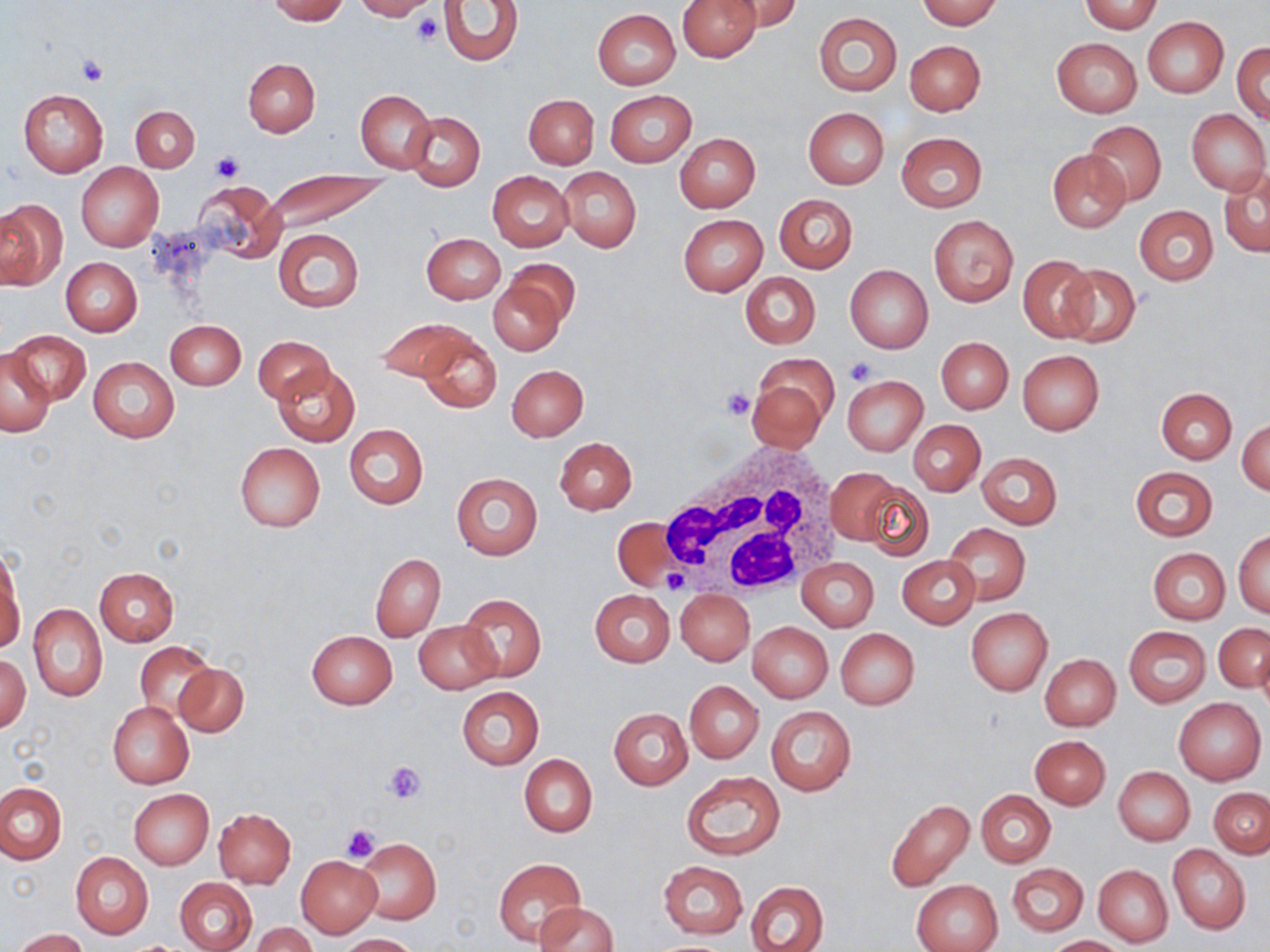 Approximate bounding boxes as [x1, y1, x2, y2] in pixels. White blood cell locations: [656, 441, 848, 603]. Platelet locations: [410, 12, 443, 45], [75, 55, 109, 87], [209, 152, 243, 184], [846, 356, 878, 383], [721, 389, 755, 422], [662, 571, 689, 594], [385, 762, 427, 804], [341, 824, 381, 862]. Uninfected red blood cell locations: [267, 0, 349, 23], [352, 0, 437, 20], [438, 0, 524, 67], [676, 0, 759, 61], [721, 0, 805, 31], [915, 0, 1001, 29], [1079, 2, 1164, 33], [593, 10, 679, 88], [813, 12, 902, 96], [1142, 18, 1228, 98], [1052, 38, 1142, 117], [905, 40, 986, 115], [1233, 42, 1270, 125], [243, 59, 319, 137], [18, 88, 109, 177], [355, 89, 437, 174], [605, 90, 696, 165], [524, 94, 598, 168], [130, 105, 199, 172], [802, 107, 888, 189], [1187, 108, 1268, 195], [405, 111, 485, 190], [1082, 120, 1166, 207], [896, 132, 986, 213], [676, 133, 760, 212], [1048, 149, 1129, 232], [77, 163, 164, 251], [559, 167, 641, 251], [1218, 167, 1270, 258], [264, 171, 392, 232], [487, 171, 573, 252], [192, 180, 285, 262], [775, 194, 858, 274], [0, 198, 66, 290], [1134, 205, 1218, 286], [678, 214, 767, 295], [929, 215, 1018, 307], [275, 229, 363, 311], [423, 233, 505, 304], [1019, 255, 1098, 341], [61, 257, 142, 336], [504, 259, 581, 327], [1056, 264, 1139, 349], [845, 265, 933, 353], [741, 272, 820, 349], [489, 277, 567, 356], [375, 318, 468, 381], [165, 320, 246, 390], [8, 330, 89, 406], [417, 332, 501, 413], [253, 335, 333, 404], [936, 337, 1012, 414], [1, 350, 56, 436], [1017, 350, 1106, 435], [87, 357, 180, 443], [746, 362, 835, 452], [272, 364, 359, 447], [506, 364, 588, 441], [843, 375, 927, 455], [1156, 387, 1236, 464], [1237, 417, 1270, 495], [909, 419, 986, 496], [344, 424, 428, 509], [554, 437, 637, 514], [234, 442, 326, 532], [977, 451, 1061, 530], [1129, 466, 1219, 542], [826, 469, 901, 547], [451, 472, 542, 560], [862, 480, 934, 561], [613, 517, 682, 592], [944, 523, 1030, 604], [1234, 530, 1270, 618], [1148, 547, 1230, 625], [1, 548, 24, 649], [370, 554, 446, 642], [898, 555, 980, 629], [797, 558, 878, 631], [95, 567, 179, 645], [589, 589, 675, 667], [676, 589, 754, 665], [459, 595, 546, 683], [30, 605, 106, 701], [966, 608, 1053, 697], [415, 621, 500, 692], [748, 622, 833, 702], [1214, 622, 1269, 692], [1124, 626, 1211, 708], [835, 629, 919, 709], [307, 630, 397, 709], [136, 642, 215, 721], [1, 651, 31, 733], [1039, 653, 1121, 731], [176, 663, 249, 737], [685, 681, 763, 763], [457, 687, 544, 769], [1173, 697, 1266, 785], [107, 701, 194, 789], [765, 705, 857, 796], [608, 707, 692, 790], [1030, 735, 1110, 809], [519, 754, 597, 836], [1113, 766, 1195, 846], [680, 771, 786, 860], [0, 782, 65, 865], [1208, 788, 1269, 857], [129, 789, 213, 869], [975, 790, 1056, 868], [885, 798, 975, 892], [213, 808, 296, 887], [354, 837, 440, 925], [1168, 845, 1250, 933], [70, 852, 153, 939], [296, 855, 381, 937], [494, 858, 585, 946], [657, 860, 748, 939], [1008, 863, 1088, 936], [1093, 864, 1173, 948], [175, 877, 258, 952], [913, 879, 1002, 952], [746, 881, 828, 952], [535, 901, 618, 951], [249, 922, 319, 952], [11, 928, 89, 952], [340, 933, 419, 951], [1046, 935, 1129, 951]. Slide-level diagnosis: no evidence of blood parasites. Light microscopy. Image is 1270×952 pixels. Thin blood smear. Captured at 1000x magnification. Single field of view. May-Grünwald-Giemsa-stained preparation.